Classify this cell by malaria status.
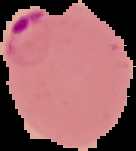
Parasitized.

{
  "image_type": "segmented cell region with the area outside set to black",
  "preparation": "thin blood smear",
  "image_size": "136×151 pixels"
}